Outline each uninfected red blood cell.
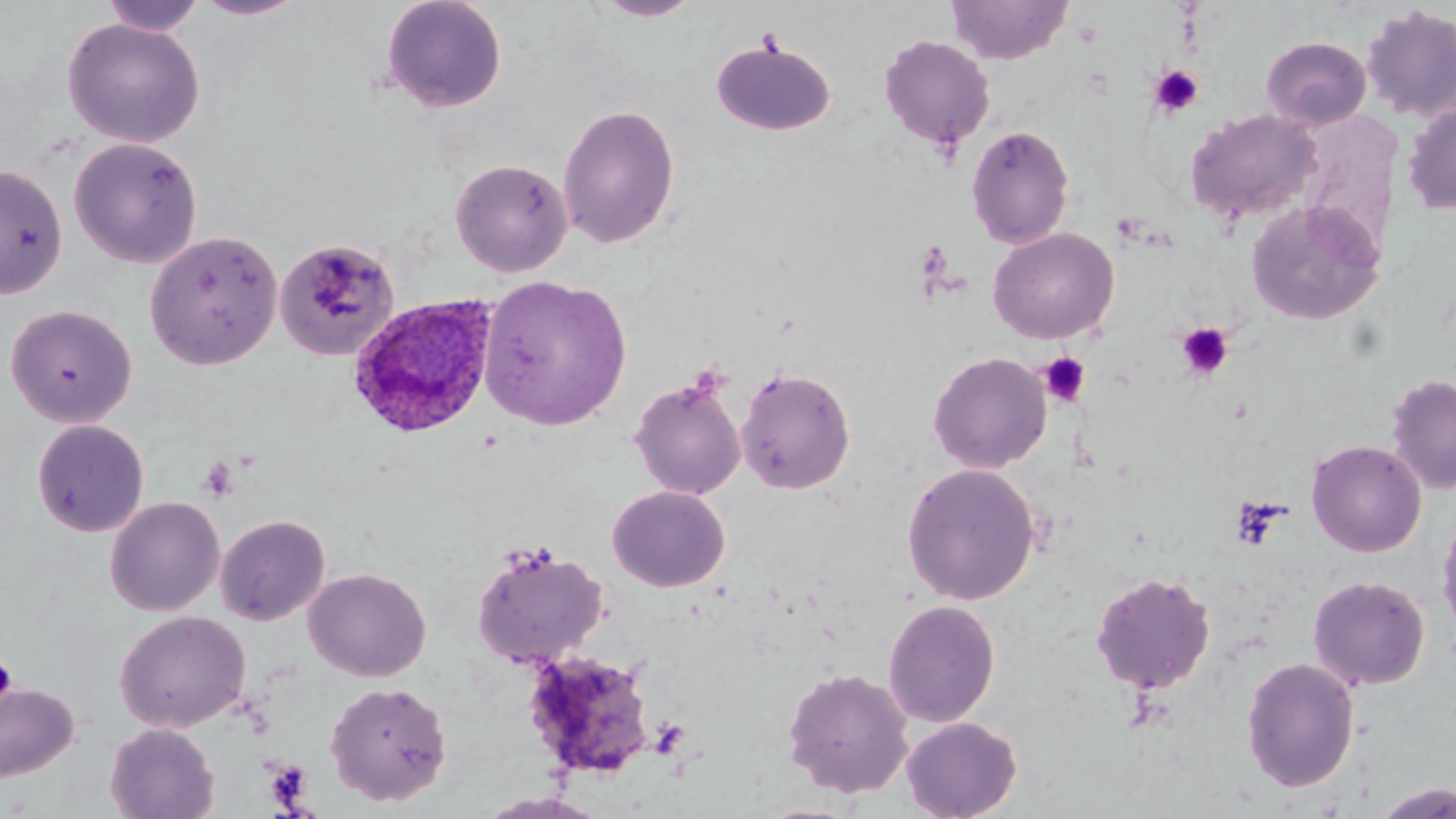

Approximate bounding boxes as [x1, y1, x2, y2] in pixels.
Uninfected red blood cells: [192, 0, 308, 21], [378, 0, 509, 114], [593, 0, 704, 21], [945, 0, 1073, 65], [101, 1, 205, 36], [1360, 5, 1456, 124], [61, 17, 206, 148], [879, 34, 996, 152], [1260, 35, 1372, 131], [711, 38, 836, 137], [1402, 98, 1456, 215], [557, 102, 681, 250], [1185, 108, 1321, 226], [965, 124, 1075, 249], [68, 136, 203, 268], [450, 157, 574, 277], [0, 163, 68, 300], [1245, 198, 1384, 326], [988, 227, 1119, 344], [144, 229, 283, 370], [273, 237, 402, 362], [478, 274, 632, 430], [4, 303, 138, 428], [928, 351, 1052, 473], [736, 366, 856, 495], [1385, 374, 1456, 495], [629, 375, 746, 500], [30, 418, 150, 538], [1306, 439, 1427, 557], [902, 462, 1041, 605], [608, 486, 730, 592], [104, 496, 225, 616], [1436, 509, 1456, 641], [214, 513, 331, 626], [471, 542, 609, 668], [303, 567, 431, 682], [1090, 571, 1216, 694], [1308, 574, 1430, 690], [882, 599, 1000, 727], [114, 610, 252, 733], [522, 649, 657, 781], [1240, 656, 1360, 793], [781, 666, 914, 799], [324, 680, 453, 805], [0, 681, 80, 782], [901, 716, 1022, 819], [105, 722, 220, 819], [1374, 782, 1456, 819], [477, 791, 610, 819].

slide-level diagnosis = Plasmodium ovale
image size = 1456×819 pixels
Plasmodium ovale-infected red blood cell locations = approximate bounding boxes as [x1, y1, x2, y2] in pixels: [347, 293, 498, 441]
field of view = single
stain = May-Grünwald-Giemsa
preparation = thin blood film
modality = optical microscopy
platelet locations = approximate bounding boxes as [x1, y1, x2, y2] in pixels: [755, 28, 786, 57], [1149, 64, 1204, 119], [914, 240, 953, 284], [1176, 322, 1233, 380], [1039, 353, 1090, 407], [198, 457, 238, 502], [1230, 495, 1288, 551], [0, 657, 17, 705], [647, 716, 690, 759], [262, 757, 314, 811]
magnification = 1000x